Describe the morphology of the erythrocytes.
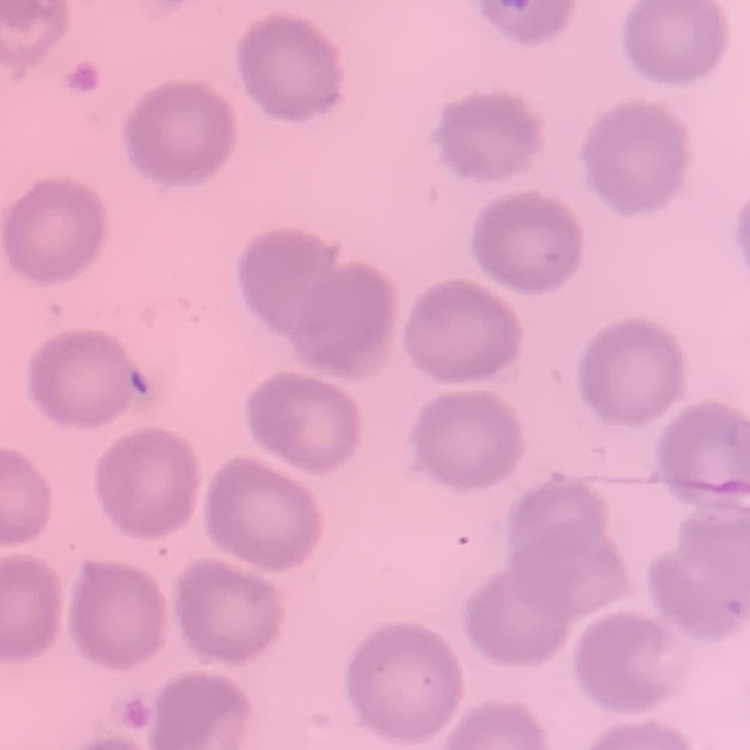

No rouleaux formation.

{
  "image_type": "one tile cut from a larger photomicrograph",
  "stain": "Field's or Giemsa",
  "preparation": "thin blood film"
}